Report the malaria status of this cell.
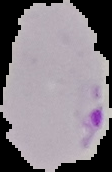
It is parasitized.

{
  "image_size": "112×172 pixels",
  "preparation": "thin blood smear",
  "image_type": "cell region segmented out of the field of view; surrounding area masked to black"
}